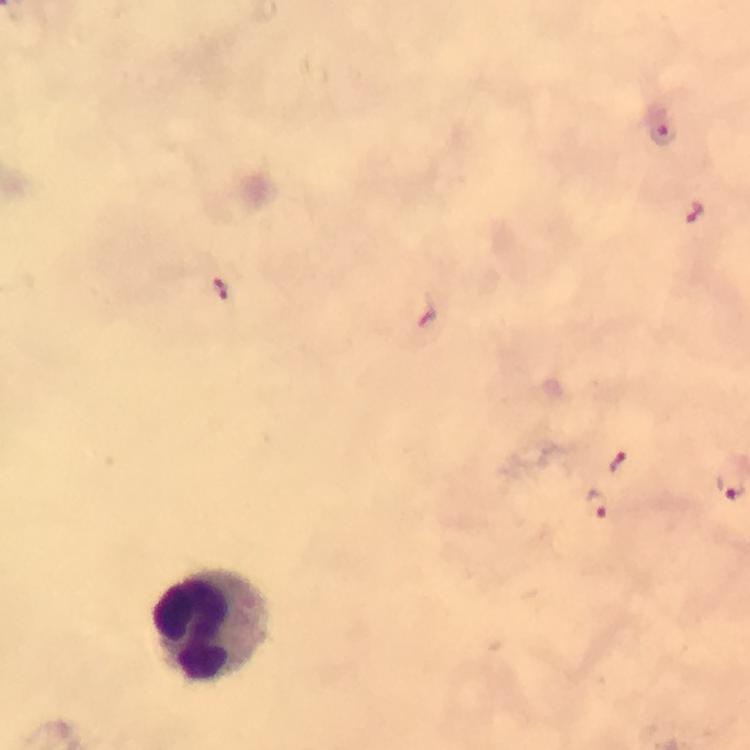
Approximate centers as {x, y} in pixels.
Summary:
  - Plasmodium parasite locations: {663, 133}, {697, 212}, {223, 289}, {428, 314}, {618, 462}, {599, 506}
  - Leukocyte locations: {211, 628}
  - Capture: smartphone camera through the microscope
  - Image size: 750×750 pixels
  - Magnification: 100x
  - Cropped from: one field of view
  - Preparation: thick smear
  - Context: from a malaria diagnostic workup
  - Stain: Giemsa
  - Immersion oil: used